Locate every blood parasite and identify its species.
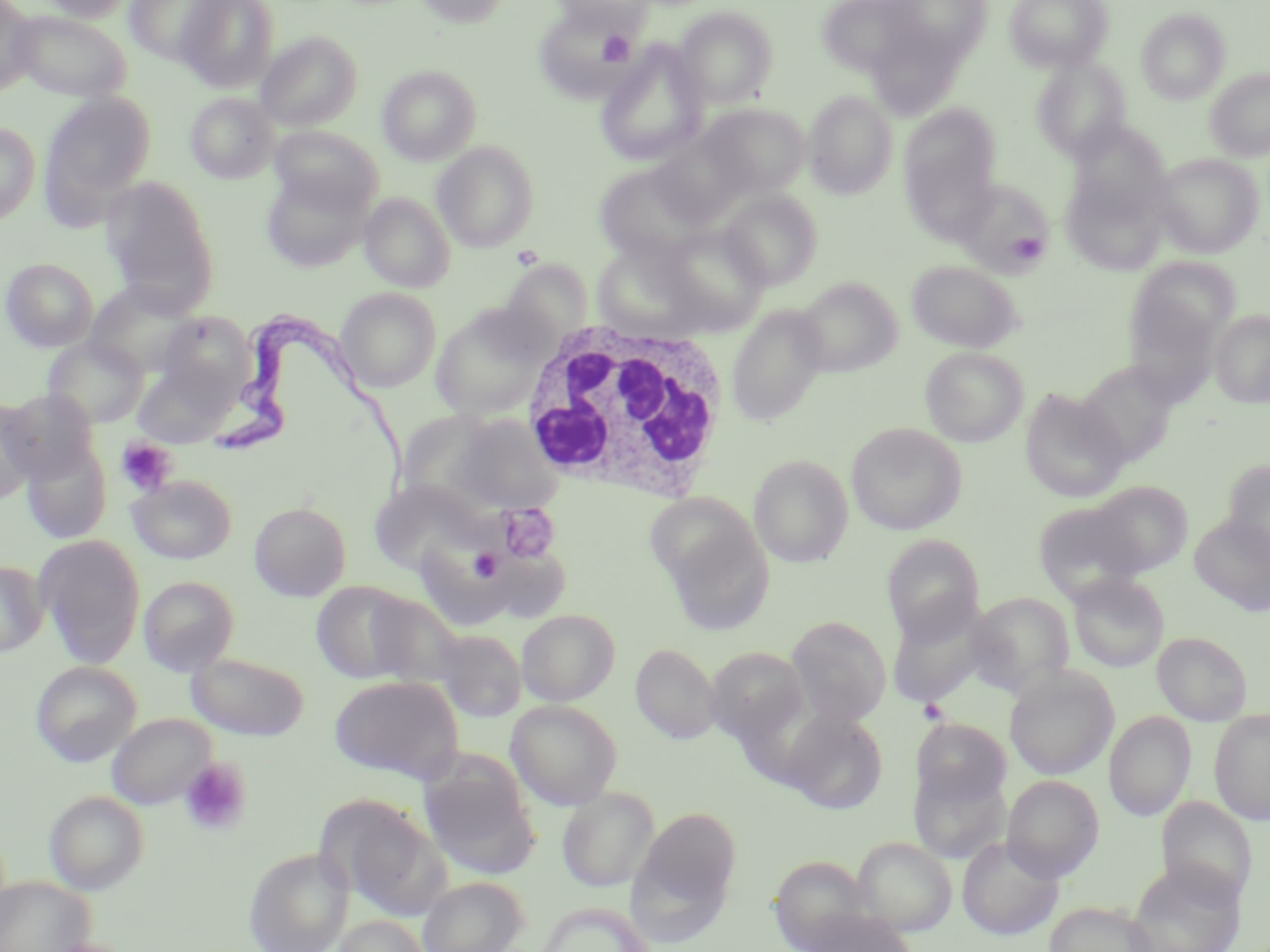

Approximate bounding boxes as [x1, y1, x2, y2] in pixels.
Trypanosoma brucei: [209, 313, 412, 485].
No Plasmodium falciparum, Plasmodium ovale, Plasmodium malariae, Plasmodium vivax, or Babesia divergens observed.

{
  "slide_level_diagnosis": "Trypanosoma brucei",
  "platelet_locations": "approximate bounding boxes as [x1, y1, x2, y2] in pixels: [597, 29, 635, 67], [1011, 232, 1045, 261], [511, 245, 543, 270], [116, 438, 177, 496], [497, 503, 560, 563], [469, 547, 505, 583], [917, 698, 949, 724], [179, 758, 251, 836]",
  "magnification": "1000x",
  "image_size": "1270×952 pixels",
  "modality": "light microscopy",
  "stain": "May-Grünwald-Giemsa",
  "field_of_view": "one of a larger specimen",
  "uninfected_red_blood_cell_locations": "approximate bounding boxes as [x1, y1, x2, y2] in pixels: [0, 0, 38, 94], [35, 0, 135, 21], [176, 0, 279, 92], [414, 0, 511, 28], [550, 0, 652, 33], [816, 0, 927, 76], [883, 0, 992, 63], [1003, 0, 1113, 72], [124, 1, 231, 65], [673, 7, 778, 108], [1137, 8, 1230, 103], [10, 10, 133, 103], [866, 23, 967, 120], [256, 31, 362, 131], [596, 41, 709, 168], [1032, 57, 1130, 160], [378, 65, 482, 165], [1205, 69, 1270, 161], [804, 91, 898, 199], [42, 92, 157, 207], [185, 92, 280, 184], [700, 104, 810, 197], [898, 105, 1002, 233], [1069, 120, 1172, 213], [0, 122, 40, 225], [270, 125, 384, 216], [432, 141, 540, 252], [1151, 153, 1264, 258], [593, 162, 712, 265], [260, 171, 373, 273], [1063, 174, 1169, 275], [101, 177, 219, 312], [952, 178, 1054, 276], [719, 189, 822, 289], [360, 192, 456, 292], [657, 223, 771, 334], [591, 244, 706, 337], [1128, 256, 1239, 359], [1, 258, 98, 352], [906, 260, 1022, 353], [795, 277, 902, 376], [85, 281, 200, 379], [1120, 285, 1226, 404], [336, 287, 441, 392], [726, 305, 829, 427], [431, 306, 549, 420], [1210, 310, 1269, 408], [159, 312, 255, 400], [44, 337, 148, 428], [920, 347, 1027, 447], [1076, 361, 1180, 467], [131, 363, 234, 448], [1019, 389, 1129, 503], [0, 398, 41, 504], [448, 412, 565, 516], [846, 423, 966, 535], [22, 436, 111, 544], [748, 454, 854, 567], [1222, 460, 1270, 562], [128, 475, 236, 564], [368, 479, 494, 577], [1090, 480, 1194, 576], [1032, 500, 1146, 602], [249, 501, 352, 601], [657, 511, 775, 636], [1189, 517, 1270, 616], [35, 535, 146, 668], [881, 535, 984, 643], [0, 560, 48, 657], [1068, 573, 1170, 672], [138, 576, 239, 676], [311, 580, 426, 685], [354, 589, 466, 688], [966, 592, 1075, 696], [886, 598, 991, 708], [517, 609, 620, 705], [786, 615, 891, 726], [432, 627, 526, 723], [1153, 632, 1252, 725], [630, 643, 721, 743], [706, 646, 809, 746], [186, 651, 310, 740], [31, 661, 142, 766], [1004, 667, 1119, 781], [330, 675, 463, 783], [506, 700, 622, 810], [780, 708, 888, 814], [1209, 709, 1270, 825], [1104, 712, 1195, 821], [107, 713, 216, 810], [911, 718, 1011, 809], [909, 761, 1010, 865], [421, 763, 540, 879], [1002, 775, 1103, 881], [558, 787, 659, 892], [45, 790, 149, 894], [1157, 797, 1257, 907], [337, 803, 452, 919], [632, 806, 742, 918], [957, 835, 1064, 940], [852, 836, 957, 935], [244, 847, 354, 952], [769, 855, 876, 952], [1126, 861, 1245, 952], [0, 876, 94, 952], [417, 876, 528, 952], [1045, 900, 1160, 952], [534, 902, 658, 952], [803, 908, 916, 952], [332, 915, 430, 952]",
  "preparation": "thin blood film",
  "white_blood_cell_locations": "approximate bounding boxes as [x1, y1, x2, y2] in pixels: [522, 317, 732, 501]"
}